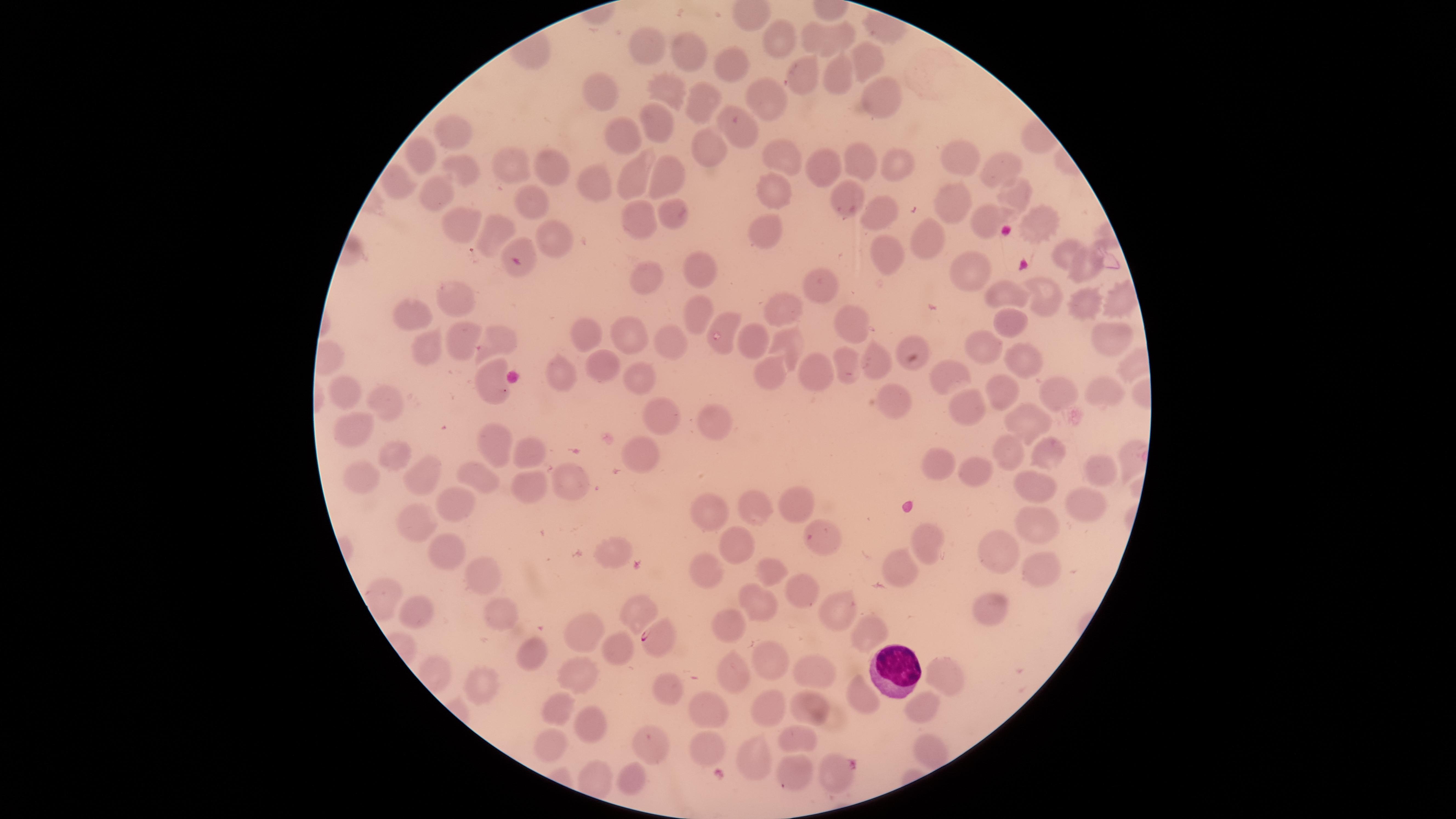
Approximate marker points as {x, y} in pixels.
Summary:
  - WBCs: {896, 669}
  - Parasitized RBCs: {518, 259}, {658, 638}, {831, 772}
  - Uninfected RBCs: {844, 36}, {780, 38}, {810, 38}, {647, 42}, {688, 52}, {732, 59}, {864, 63}, {834, 73}, {800, 75}, {604, 85}, {667, 91}, {709, 92}, {880, 97}, {762, 102}, {733, 119}, {657, 125}, {456, 131}, {623, 132}, {706, 151}, {422, 156}, {786, 159}, {858, 162}, {965, 163}, {997, 163}, {827, 165}, {522, 166}, {464, 169}, {898, 171}, {553, 173}, {660, 178}, {596, 181}, {405, 183}, {632, 184}, {1018, 189}, {777, 190}, {848, 190}, {432, 193}, {527, 194}, {955, 203}, {891, 207}, {672, 216}, {632, 219}, {990, 219}, {1039, 223}, {467, 226}, {771, 233}, {494, 234}, {547, 239}, {934, 241}, {1069, 250}, {886, 254}, {702, 264}, {977, 270}, {1084, 270}, {647, 279}, {829, 281}, {1012, 291}, {1050, 295}, {1116, 298}, {460, 299}, {1082, 304}, {787, 308}, {692, 317}, {412, 319}, {1005, 321}, {725, 323}, {853, 325}, {625, 329}, {1114, 333}, {586, 337}, {666, 338}, {786, 339}, {755, 341}, {498, 343}, {908, 345}, {459, 346}, {982, 347}, {421, 348}, {1027, 360}, {875, 363}, {850, 364}, {605, 366}, {948, 371}, {771, 373}, {559, 375}, {632, 376}, {814, 376}, {487, 379}, {1107, 387}, {343, 392}, {999, 392}, {1058, 394}, {389, 400}, {894, 401}, {966, 410}, {714, 413}, {659, 414}, {1026, 422}, {358, 431}, {495, 443}, {1017, 446}, {528, 450}, {1054, 453}, {642, 455}, {398, 457}, {943, 457}, {1100, 463}, {975, 465}, {425, 476}, {476, 476}, {364, 477}, {567, 483}, {529, 485}, {1040, 490}, {1086, 491}, {454, 502}, {795, 504}, {757, 509}, {713, 511}, {1033, 519}, {415, 527}, {926, 544}, {1001, 545}, {736, 546}, {445, 548}, {613, 550}, {710, 572}, {773, 572}, {1040, 574}, {480, 577}, {900, 577}, {798, 594}, {752, 600}, {986, 605}, {416, 610}, {836, 611}, {634, 614}, {498, 615}, {729, 625}, {589, 631}, {867, 631}, {615, 646}, {531, 657}, {771, 664}, {738, 670}, {812, 673}, {946, 673}, {581, 675}, {483, 682}, {665, 686}, {860, 697}, {917, 703}, {558, 706}, {809, 706}, {769, 707}, {707, 712}, {586, 720}, {798, 737}, {648, 741}, {556, 744}, {702, 747}, {931, 748}, {752, 752}, {791, 772}, {635, 773}
  - Image size: 1456×819 pixels
  - Preparation: thin smear of blood
  - Stain: Giemsa
  - Field of view: single
  - Presence: malaria parasites detected
  - Capture: smartphone photograph through the microscope eyepiece
  - Visible region: circular
  - Species: Plasmodium falciparum